Report the malaria status of this cell.
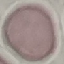

Uninfected.

Summary:
  - Image type: cell patch, automatically extracted from a larger field of view and resized to 64 × 64 pixels
  - Stain: Giemsa
  - Capture: smartphone camera at the microscope eyepiece
  - Preparation: thin blood film